Classify this cell by malaria status.
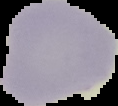
It is uninfected.

image size = 118×106 pixels
preparation = thin blood film
image type = cell region segmented out of the field of view; surrounding area masked to black